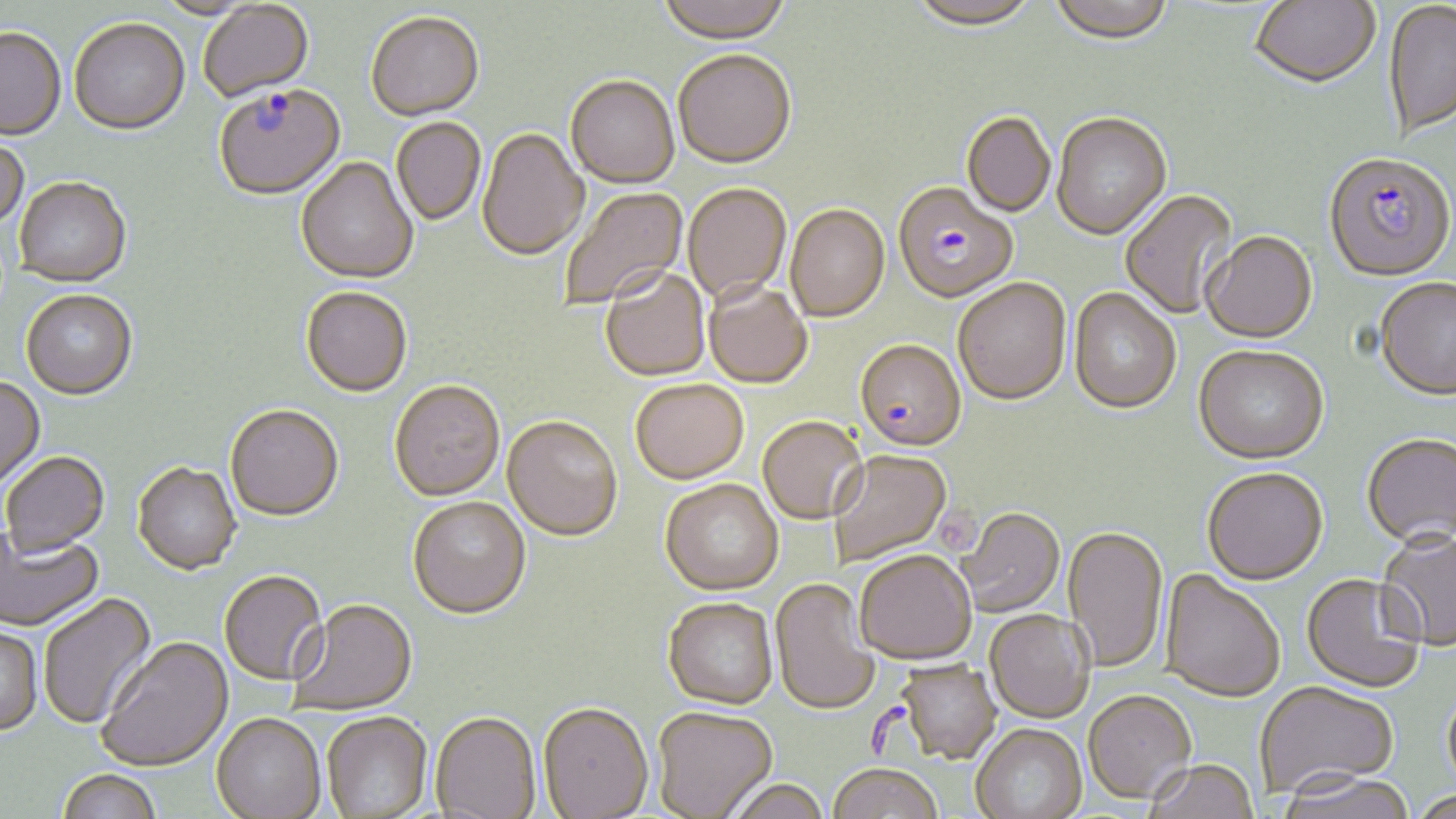

Summary:
  - Coordinate format: approximate bounding boxes as (x1,y1)-(x2,y2) corner pairs in pixels
  - Uninfected red blood cell locations: (153,0)-(260,21), (656,0)-(792,47), (1048,0)-(1175,47), (1249,0)-(1380,90), (908,1)-(1041,33), (1384,1)-(1456,140), (198,2)-(315,104), (366,14)-(485,124), (69,21)-(190,138), (0,31)-(66,144), (673,52)-(797,170), (565,78)-(679,191), (961,113)-(1056,218), (1052,115)-(1172,242), (391,119)-(486,227), (477,129)-(588,263), (0,138)-(29,233), (296,159)-(418,286), (13,179)-(132,290), (683,184)-(791,306), (559,186)-(689,312), (1119,190)-(1238,321), (785,205)-(890,325), (1201,231)-(1318,345), (600,269)-(710,382), (953,279)-(1072,406), (1375,279)-(1456,401), (704,282)-(812,389), (1068,288)-(1182,416), (301,289)-(412,399), (21,292)-(138,402), (1193,347)-(1328,466), (0,377)-(46,491), (630,380)-(749,487), (389,382)-(505,503), (225,407)-(344,524), (757,417)-(867,526), (502,418)-(623,544), (1362,434)-(1456,551), (828,451)-(952,568), (2,453)-(110,560), (132,464)-(241,578), (1202,468)-(1328,587), (660,480)-(784,598), (407,499)-(531,623), (957,509)-(1064,618), (1062,527)-(1169,673), (0,528)-(104,634), (1376,531)-(1456,649), (853,552)-(977,667), (1160,570)-(1285,704), (219,572)-(328,688), (1302,574)-(1426,694), (770,579)-(880,717), (38,593)-(158,730), (662,599)-(779,711), (290,601)-(418,717), (984,611)-(1094,724), (0,626)-(44,738), (97,637)-(234,774), (896,661)-(1000,765), (1256,682)-(1399,801), (1442,684)-(1456,802), (1083,693)-(1197,805), (537,702)-(653,819), (652,708)-(778,818), (321,713)-(432,818), (429,713)-(541,818), (211,714)-(326,819), (971,725)-(1088,819), (1145,762)-(1259,819), (827,767)-(943,819), (57,770)-(161,819), (1277,775)-(1417,819), (718,782)-(831,819), (1408,789)-(1456,818)
  - Plasmodium falciparum-infected red blood cell locations: (214,87)-(346,203), (1323,153)-(1455,284), (892,183)-(1019,304), (854,341)-(966,454)
  - Slide-level diagnosis: Plasmodium falciparum
  - Magnification: 1000x
  - Image size: 1456×819 pixels
  - Modality: optical microscopy
  - Preparation: thin blood film
  - Stain: May-Grünwald-Giemsa
  - Field of view: single